Locate every blood parasite and identify its species.
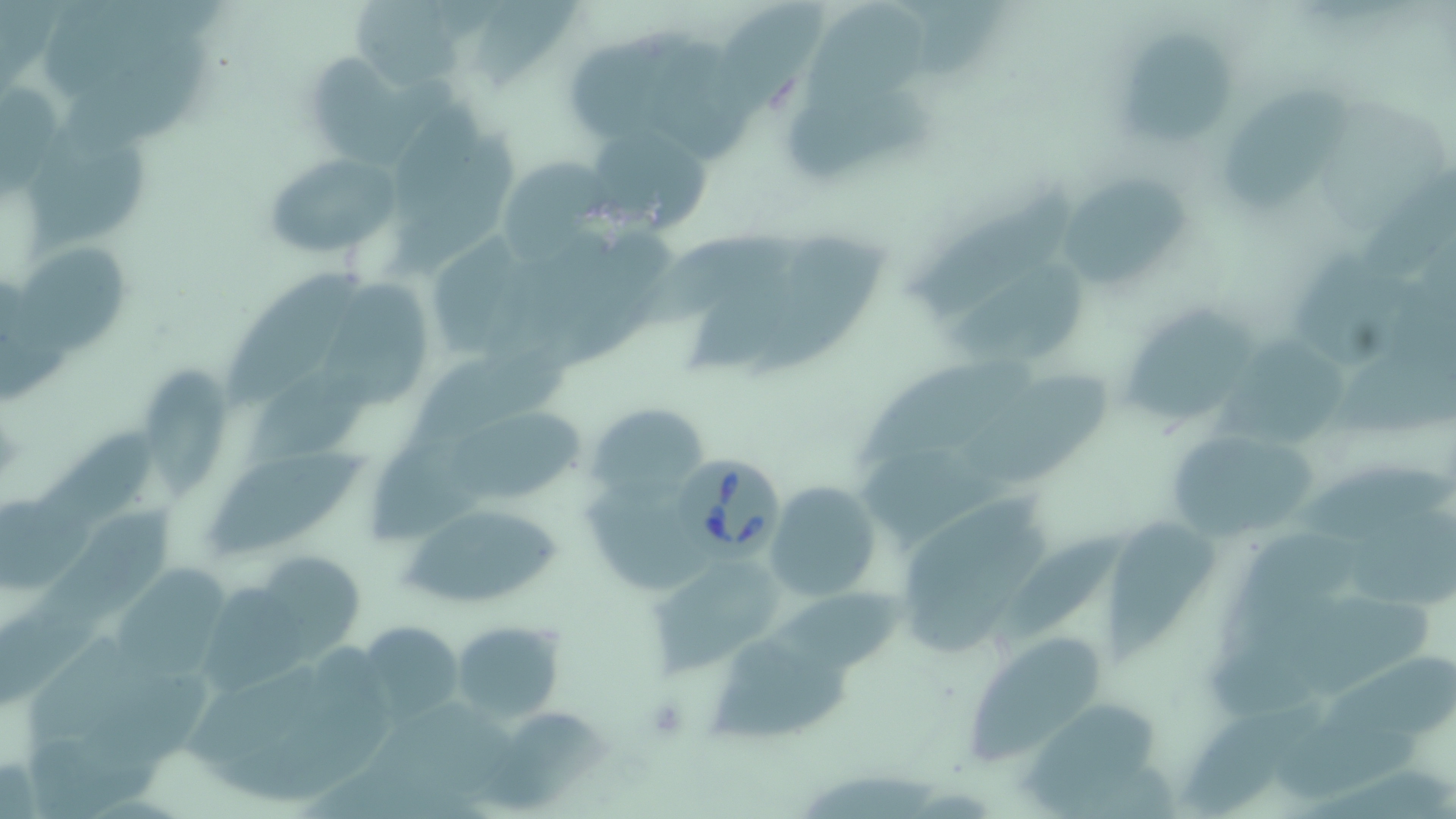

Approximate bounding boxes as named x1/y1/x2/y2 corners in pixels.
Babesia divergens-infected red blood cells: (x1=680, y1=454, x2=787, y2=562).
No Plasmodium falciparum, Plasmodium ovale, Plasmodium malariae, Plasmodium vivax, or Trypanosoma brucei observed.

slide-level diagnosis = Babesia divergens
field of view = single
preparation = thin blood smear
image size = 1456×819 pixels
stain = May-Grünwald-Giemsa
modality = optical microscopy
uninfected red blood cell locations = approximate bounding boxes as named x1/y1/x2/y2 corners in pixels: (x1=350, y1=0, x2=475, y2=93), (x1=706, y1=0, x2=823, y2=121), (x1=807, y1=5, x2=932, y2=121), (x1=1123, y1=30, x2=1231, y2=142), (x1=53, y1=33, x2=206, y2=167), (x1=652, y1=42, x2=755, y2=161), (x1=314, y1=51, x2=455, y2=163), (x1=1222, y1=82, x2=1354, y2=214), (x1=788, y1=90, x2=938, y2=184), (x1=20, y1=121, x2=146, y2=265), (x1=581, y1=123, x2=711, y2=235), (x1=262, y1=151, x2=401, y2=260), (x1=494, y1=155, x2=614, y2=261), (x1=1062, y1=173, x2=1188, y2=293), (x1=912, y1=175, x2=1078, y2=317), (x1=629, y1=232, x2=807, y2=328), (x1=739, y1=235, x2=898, y2=383), (x1=7, y1=243, x2=134, y2=363), (x1=1296, y1=249, x2=1412, y2=371), (x1=223, y1=260, x2=361, y2=406), (x1=941, y1=264, x2=1090, y2=361), (x1=319, y1=279, x2=446, y2=417), (x1=1125, y1=305, x2=1256, y2=429), (x1=1221, y1=328, x2=1352, y2=454), (x1=415, y1=348, x2=576, y2=452), (x1=856, y1=350, x2=1030, y2=475), (x1=139, y1=364, x2=234, y2=498), (x1=961, y1=368, x2=1120, y2=487), (x1=587, y1=402, x2=707, y2=503), (x1=449, y1=408, x2=586, y2=502), (x1=1167, y1=427, x2=1320, y2=541), (x1=35, y1=439, x2=156, y2=542), (x1=211, y1=442, x2=369, y2=567), (x1=860, y1=445, x2=1019, y2=544), (x1=1299, y1=461, x2=1453, y2=542), (x1=764, y1=480, x2=882, y2=602), (x1=584, y1=481, x2=709, y2=590), (x1=32, y1=501, x2=178, y2=644), (x1=397, y1=501, x2=570, y2=612), (x1=1346, y1=508, x2=1456, y2=609), (x1=1108, y1=511, x2=1219, y2=663), (x1=995, y1=526, x2=1125, y2=656), (x1=647, y1=555, x2=787, y2=672), (x1=121, y1=557, x2=238, y2=682), (x1=776, y1=583, x2=931, y2=676), (x1=202, y1=585, x2=316, y2=696), (x1=358, y1=618, x2=466, y2=724), (x1=450, y1=620, x2=563, y2=723), (x1=971, y1=634, x2=1106, y2=767), (x1=709, y1=638, x2=855, y2=743), (x1=1333, y1=654, x2=1456, y2=743), (x1=187, y1=662, x2=325, y2=765), (x1=1179, y1=700, x2=1324, y2=812), (x1=489, y1=702, x2=609, y2=813), (x1=1021, y1=702, x2=1158, y2=810)
magnification = 1000x